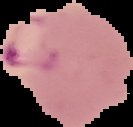 Image is 133×127 pixels. Result: malaria parasites identified. From a thin blood smear. Segmented cell region on a black background.